Comment on the morphology of the red blood cells.
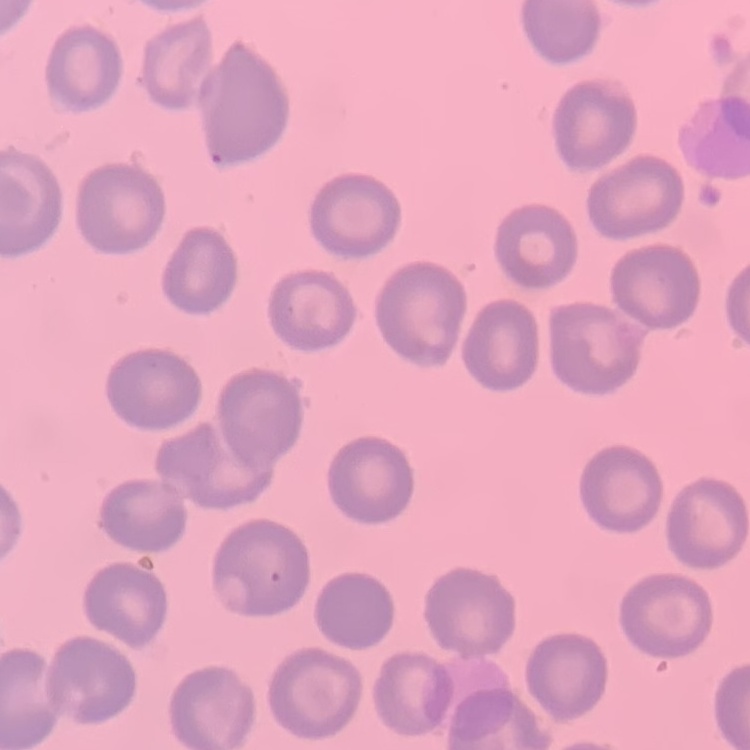
No rouleaux formation.

Square crop of a larger photomicrograph. Thin blood film. Stained with either Field's or Giemsa.